Give the position of every leukocyte visible.
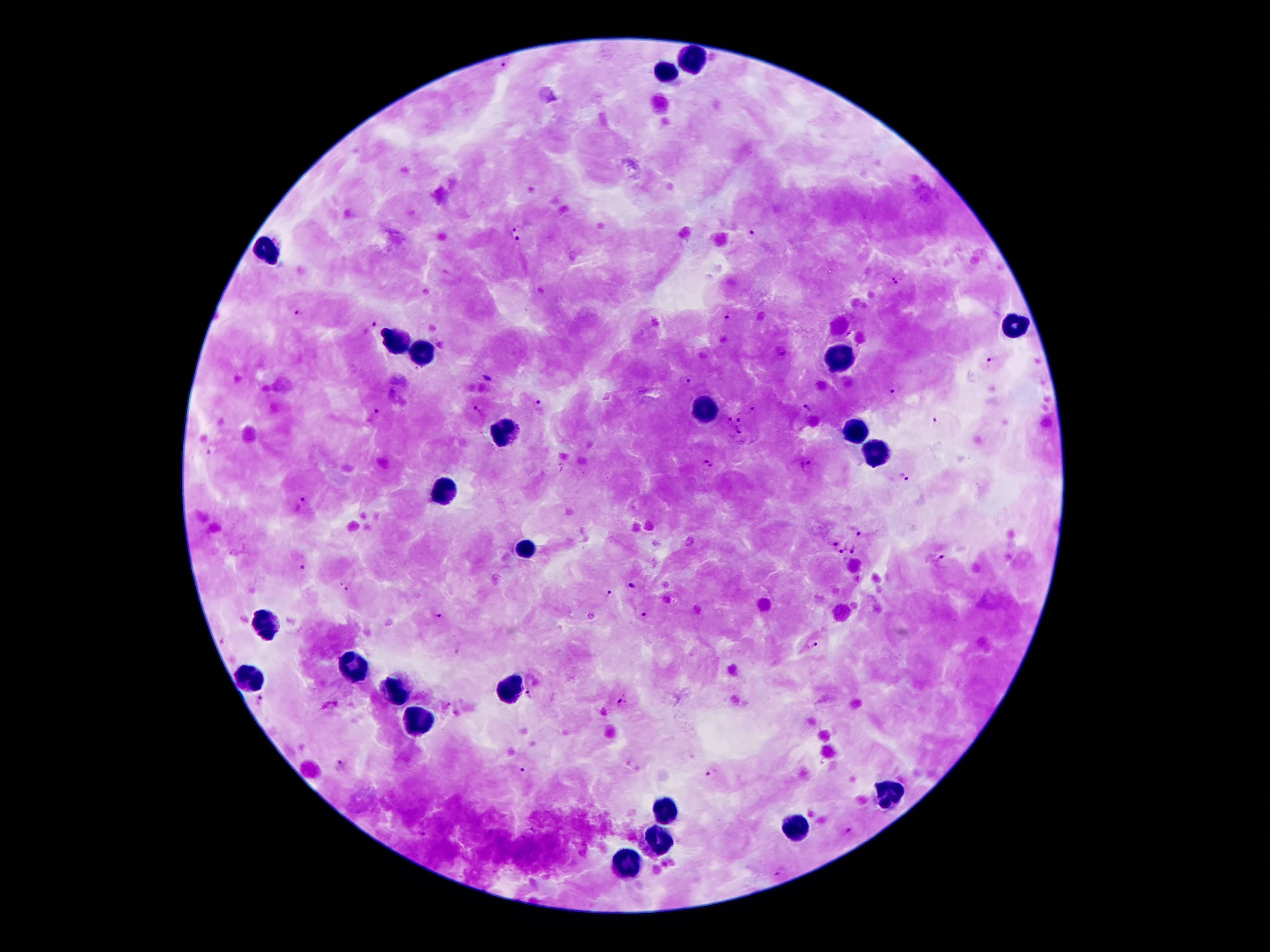

Approximate centers as {x, y} in pixels.
Leukocytes: {695, 60}, {667, 72}, {264, 249}, {1011, 328}, {395, 344}, {420, 355}, {838, 355}, {702, 411}, {855, 428}, {502, 434}, {877, 454}, {440, 496}, {526, 549}, {264, 620}, {356, 669}, {252, 678}, {509, 690}, {393, 692}, {418, 722}, {887, 791}, {665, 810}, {796, 830}, {657, 838}, {625, 867}.

Malaria parasite locations: {518, 228}, {756, 230}, {513, 241}, {897, 280}, {300, 312}, {728, 317}, {373, 325}, {782, 352}, {991, 362}, {487, 376}, {689, 383}, {895, 390}, {539, 405}, {751, 410}, {806, 410}, {477, 411}, {376, 414}, {740, 419}, {728, 422}, {936, 423}, {739, 432}, {211, 450}, {708, 464}, {806, 466}, {903, 476}, {301, 503}, {858, 531}, {830, 541}, {855, 549}, {842, 551}, {941, 560}, {300, 566}, {634, 584}, {346, 587}, {608, 594}, {645, 614}, {437, 615}, {812, 643}, {528, 696}, {259, 701}, {620, 704}, {341, 765}, {523, 769}, {710, 774}, {531, 829}, {847, 830}, {491, 833}, {423, 834}, {523, 839}, {778, 872}. Giemsa stain. Patient malaria status: infected with Plasmodium falciparum. One field from this slide. 100x magnification. Smartphone photograph taken through the microscope eyepiece. Image is 1270×952 pixels. Thick peripheral-blood smear.